Assess the morphology of the red blood cells.
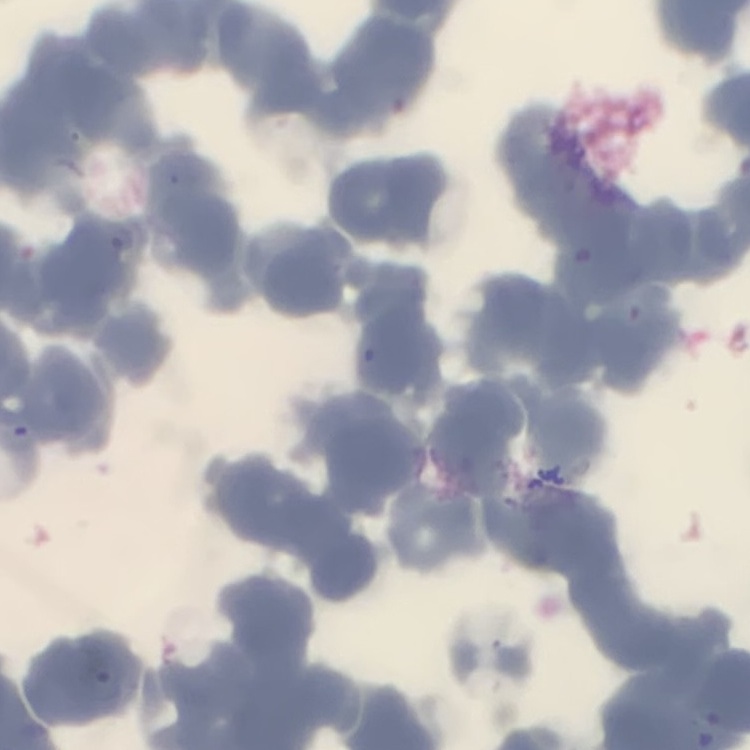

Rouleaux formation.

Thin peripheral smear. Stained with either Field's or Giemsa. Square crop of a larger photomicrograph.